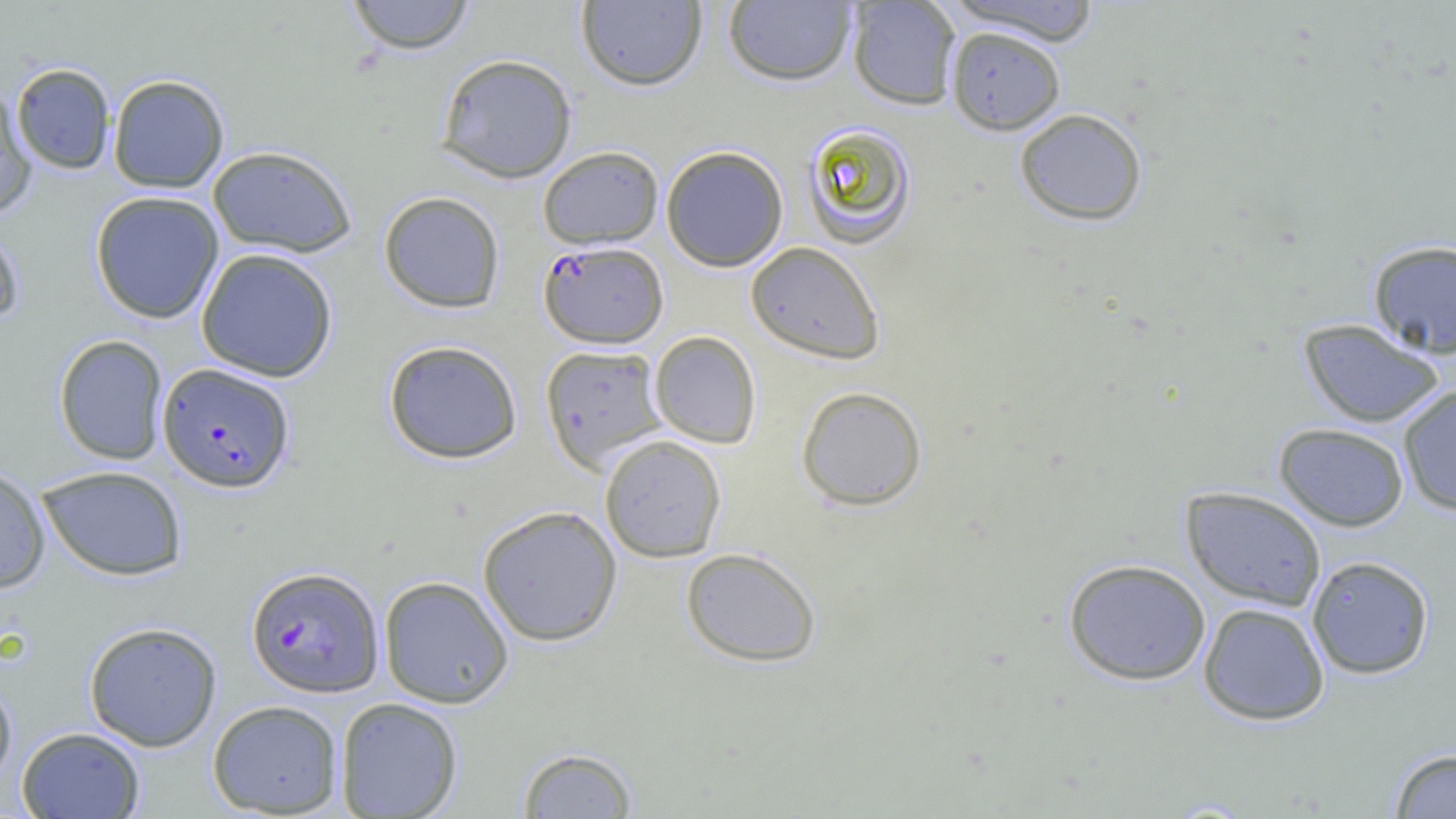
Approximate bounding boxes as (x1, y1, x2, y2) in pixels. Plasmodium falciparum-infected red blood cell locations: (539, 240, 668, 348), (157, 362, 295, 493), (245, 566, 384, 698). Uninfected red blood cell locations: (343, 0, 477, 55), (847, 0, 962, 110), (576, 1, 707, 91), (723, 1, 858, 87), (945, 1, 1104, 46), (945, 25, 1066, 135), (435, 53, 578, 183), (10, 63, 117, 174), (107, 74, 230, 193), (0, 89, 38, 218), (1014, 107, 1148, 226), (800, 122, 918, 250), (207, 145, 358, 258), (537, 145, 664, 249), (661, 145, 789, 272), (89, 190, 225, 324), (378, 190, 506, 313), (0, 220, 25, 330), (1367, 239, 1456, 359), (744, 241, 886, 365), (195, 248, 338, 382), (1297, 318, 1447, 428), (649, 330, 762, 449), (53, 334, 169, 465), (382, 339, 523, 464), (539, 344, 669, 472), (1397, 384, 1456, 517), (796, 385, 928, 511), (1274, 422, 1410, 531), (599, 435, 727, 563), (0, 462, 51, 593), (36, 465, 188, 581), (1180, 486, 1328, 611), (477, 505, 623, 646), (680, 546, 822, 667), (1306, 555, 1435, 679), (1062, 558, 1211, 685), (378, 575, 514, 708), (1198, 602, 1330, 725), (83, 621, 222, 751), (0, 677, 18, 792), (335, 697, 463, 819), (207, 699, 344, 817), (16, 726, 145, 818), (516, 746, 638, 818), (1388, 747, 1456, 818). Slide-level diagnosis: Plasmodium falciparum. 1000x magnification. Image is 1456×819 pixels. Thin blood smear. Light microscopy. Single field of view.